Classify this cell by malaria status.
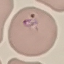
It is parasitized.

Giemsa stain. Thin smear of blood. Acquired by smartphone through the microscope eyepiece. Cell patch, automatically extracted from a larger field of view and resized to 64 × 64 pixels.